State the blood parasite species.
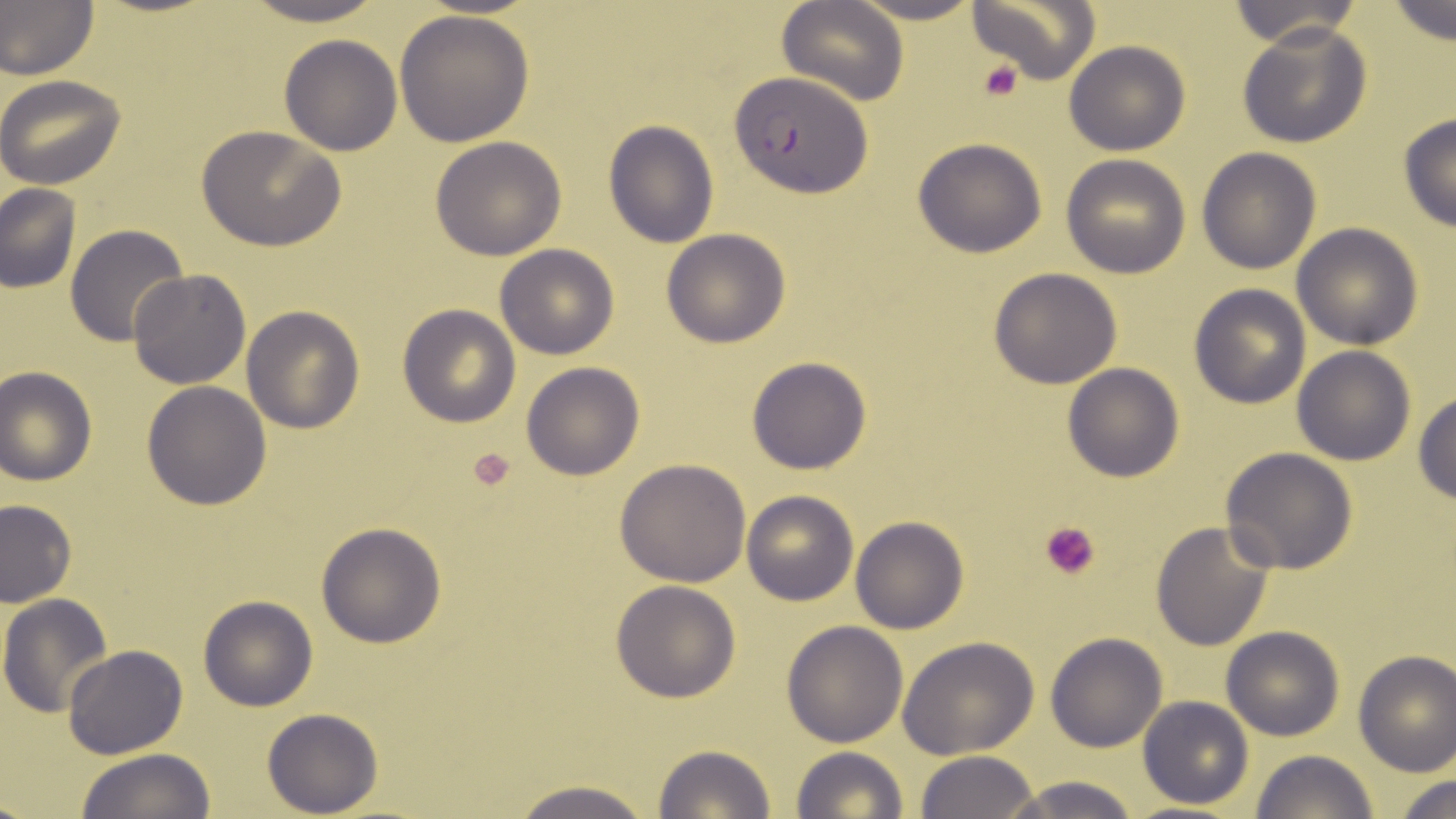

Plasmodium falciparum.

Approximate bounding boxes as [x1, y1, x2, y2] in pixels. Uninfected red blood cell locations: [232, 0, 395, 26], [777, 0, 910, 105], [848, 0, 987, 25], [969, 0, 1100, 86], [1386, 0, 1455, 47], [1227, 1, 1362, 46], [0, 2, 98, 79], [394, 7, 535, 147], [1237, 22, 1373, 150], [278, 34, 401, 155], [1064, 40, 1190, 156], [0, 73, 126, 189], [1397, 112, 1456, 232], [604, 121, 718, 248], [195, 125, 345, 250], [430, 136, 568, 260], [913, 137, 1050, 258], [1196, 147, 1321, 274], [1060, 155, 1191, 278], [0, 182, 81, 293], [1291, 223, 1424, 350], [65, 225, 191, 348], [661, 229, 792, 348], [495, 243, 619, 360], [989, 268, 1123, 388], [128, 269, 252, 390], [1188, 284, 1310, 408], [398, 303, 522, 427], [241, 305, 365, 433], [1292, 346, 1416, 465], [746, 355, 873, 475], [521, 361, 645, 480], [1062, 363, 1185, 482], [0, 364, 97, 485], [141, 381, 272, 511], [1413, 392, 1456, 506], [1219, 447, 1357, 573], [614, 458, 752, 587], [740, 491, 859, 606], [0, 498, 78, 607], [850, 516, 968, 634], [1150, 521, 1274, 650], [316, 522, 446, 648], [610, 580, 741, 702], [1, 595, 116, 718], [199, 595, 317, 711], [781, 620, 907, 748], [1221, 626, 1344, 741], [1045, 633, 1166, 752], [897, 636, 1041, 757], [64, 644, 188, 758], [1353, 649, 1456, 777], [1137, 696, 1255, 808], [261, 708, 383, 816], [651, 744, 777, 819], [790, 747, 908, 819], [75, 749, 214, 819], [1250, 749, 1379, 819], [913, 751, 1040, 819], [1392, 773, 1456, 818], [995, 774, 1148, 818], [505, 779, 660, 819]. Plasmodium falciparum-infected red blood cell locations: [729, 72, 871, 197]. Platelet locations: [976, 58, 1027, 103], [465, 446, 521, 494], [1041, 521, 1099, 581]. May-Grünwald-Giemsa-stained preparation. Light microscopy. Image is 1456×819 pixels. Single field of view. Captured at 1000x magnification. Thin blood smear.